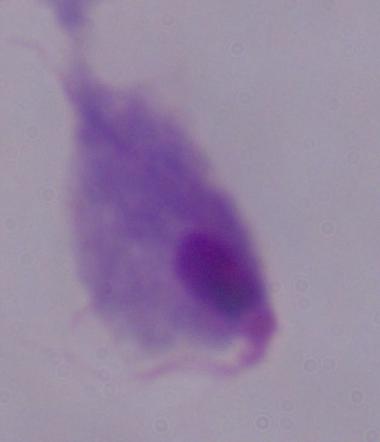
Captured at 1000x magnification. Photomicrograph. A trichomonad is seen.